Point out each Plasmodium parasite.
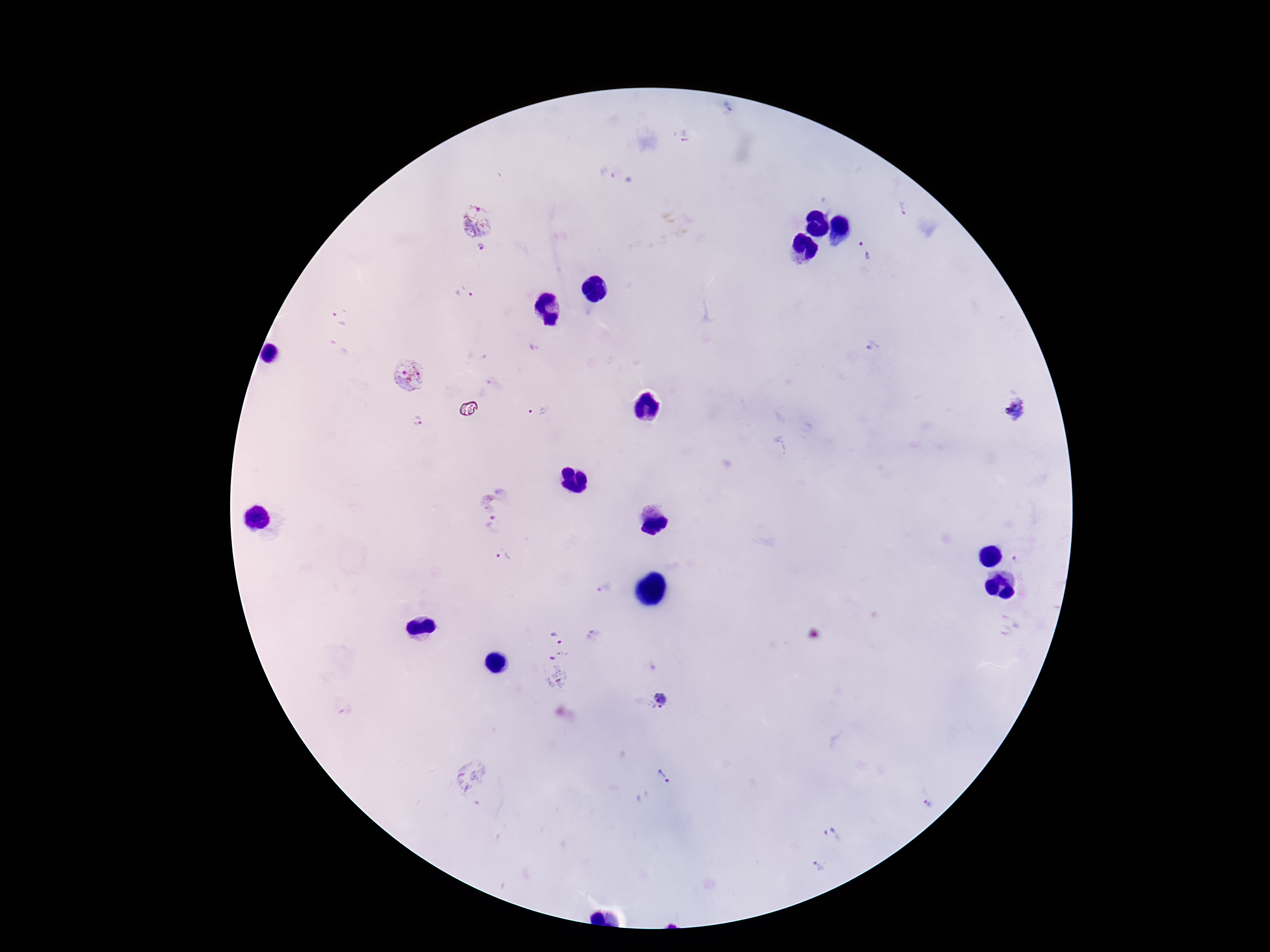
Approximate object centers, in pixels from the top-left corner.
Plasmodium parasites: (x=686, y=137), (x=607, y=174), (x=901, y=208), (x=478, y=220), (x=481, y=248), (x=864, y=249), (x=463, y=295), (x=340, y=317), (x=340, y=346), (x=872, y=348), (x=409, y=376), (x=1017, y=407), (x=536, y=410), (x=418, y=422), (x=496, y=511), (x=504, y=558), (x=1015, y=558), (x=604, y=591), (x=593, y=635), (x=558, y=638), (x=554, y=672), (x=665, y=699), (x=468, y=776), (x=666, y=777), (x=928, y=804), (x=828, y=828), (x=821, y=864).

100x magnification. One field from this slide. Patient malaria status: positive. Thick blood smear. Smartphone photograph taken through the microscope eyepiece. Image is 1270×952 pixels. Giemsa stain.